Identify the parasite.
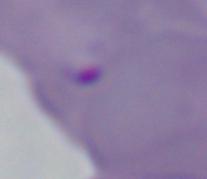
Babesia.

1000x magnification. Micrograph.